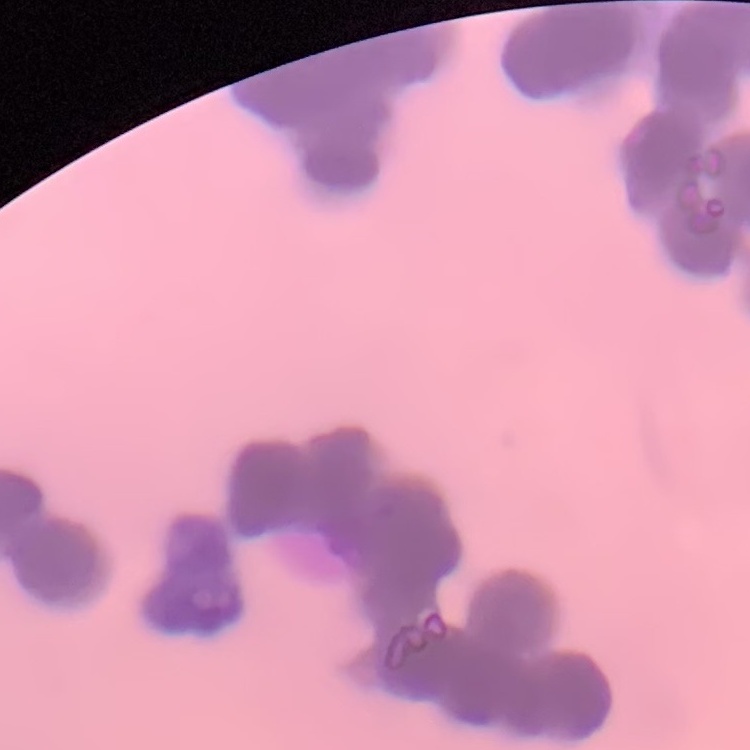

red blood cell morphology = rouleaux formation
preparation = thin peripheral smear
image type = one tile cut from a larger photomicrograph
stain = Field's or Giemsa